Assess the morphology of the red blood cells.
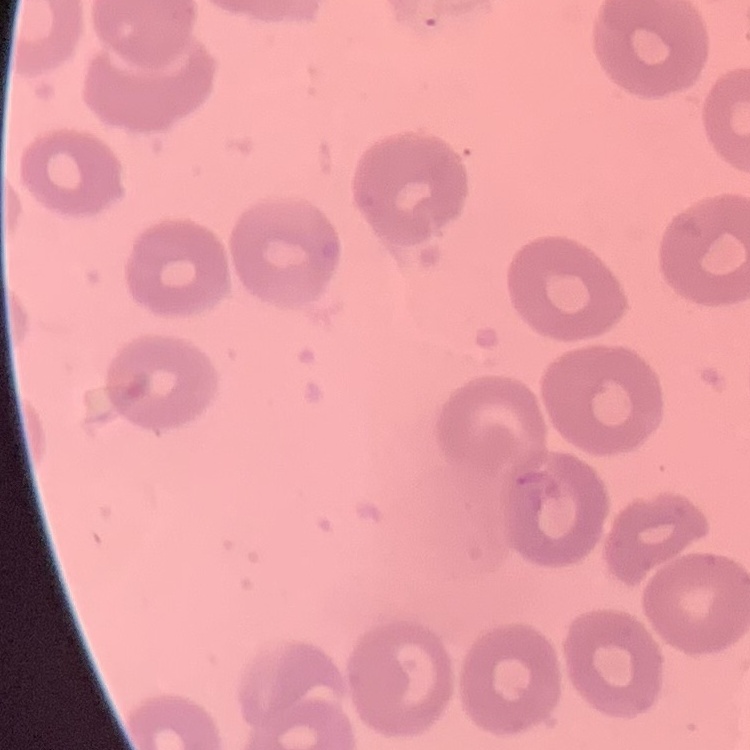

They show no rouleaux formation.

Stained with either Field's or Giemsa. One tile cut from a larger photomicrograph. Thin blood smear.